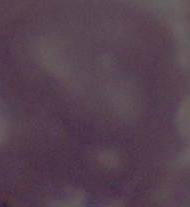
modality = micrograph
magnification = 1000x
identification = erythrocyte